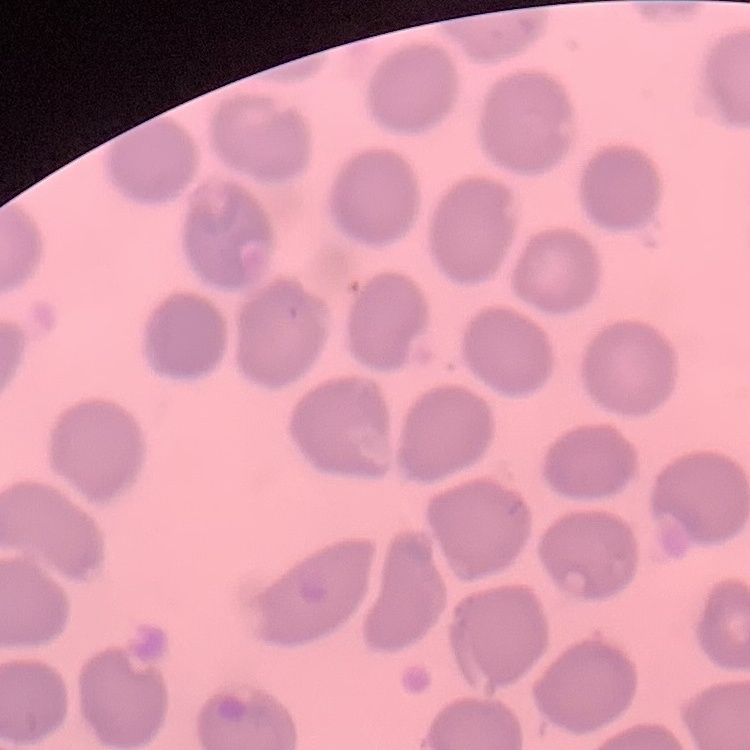

{
  "erythrocyte_morphology": "no rouleaux formation",
  "image_type": "square crop of a larger photomicrograph",
  "preparation": "thin peripheral smear",
  "stain": "Field's or Giemsa"
}